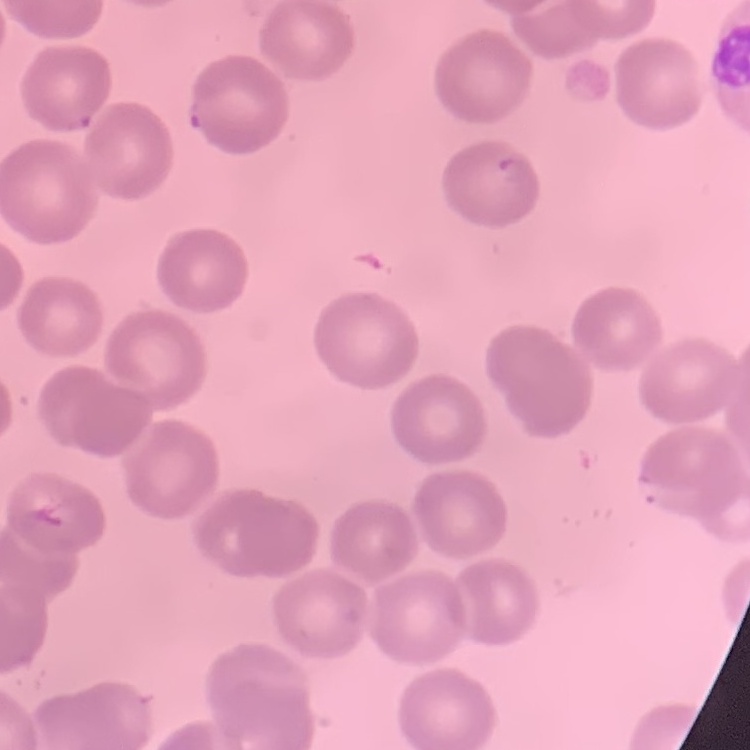
erythrocyte_morphology: no rouleaux formation
image_type: square crop of a larger photomicrograph
stain: Field's or Giemsa
preparation: thin blood film